Classify this cell by malaria status.
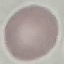

It is uninfected.

Summary:
  - Image type: cell patch, automatically extracted from a larger field of view and resized to 64 × 64 pixels
  - Capture: smartphone through the microscope eyepiece
  - Preparation: thin blood film
  - Stain: Giemsa